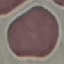

malaria status = uninfected
preparation = thin smear
capture = smartphone through the microscope eyepiece
stain = Giemsa
image type = automatically extracted cell patch, resized to 64 × 64 pixels